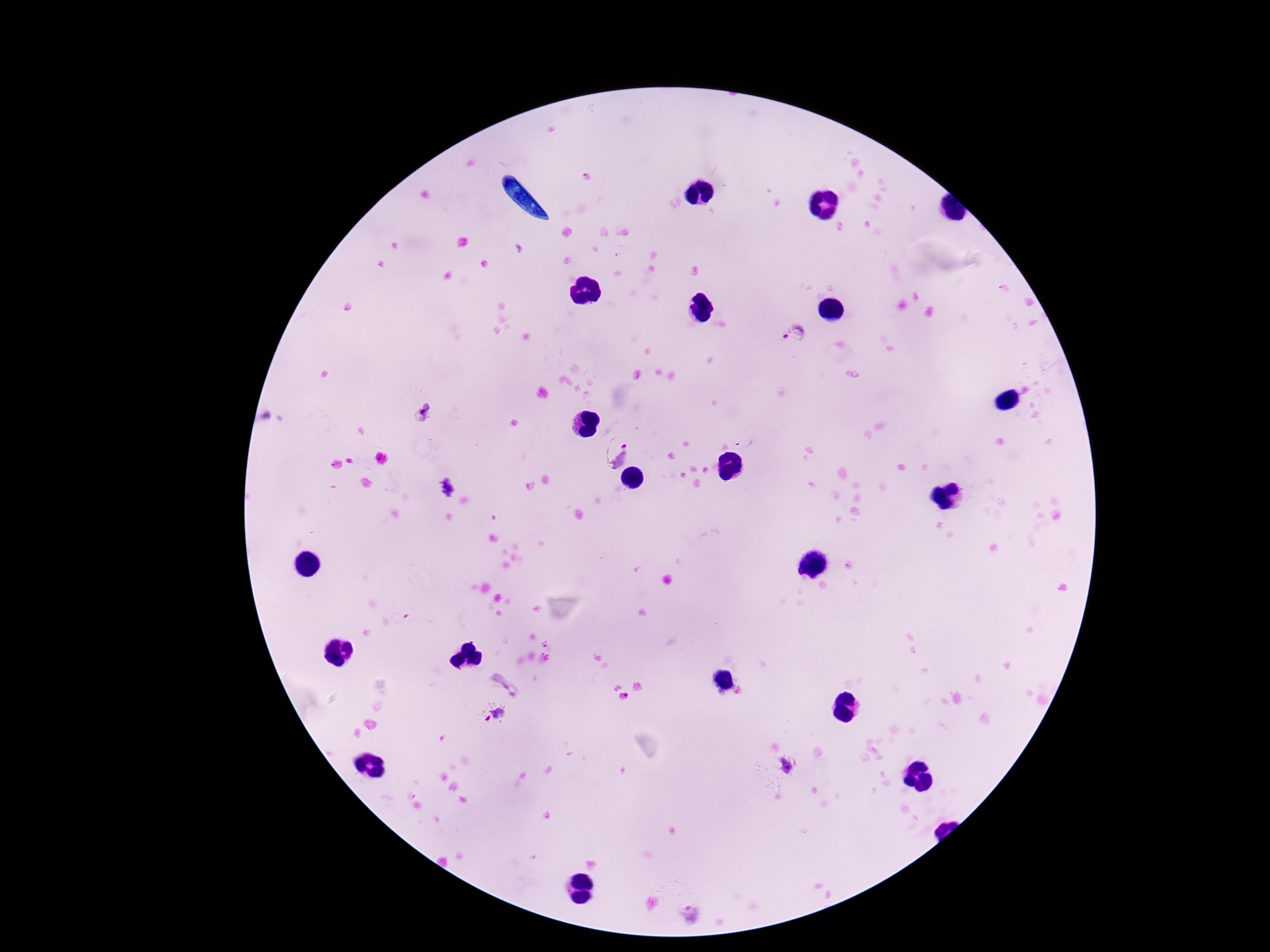

image_size: 1270×952 pixels
field_of_view: single
patient_malaria_status: infected
plasmodium_parasite_locations: 'approximate centers as {x, y} in pixels: {795, 336}, {424, 413}, {615, 451}, {445, 487}, {506, 684}, {493, 713}, {789, 765}, {690, 915}'
preparation: thick blood film
magnification: 100x
stain: Giemsa
capture: smartphone camera through the microscope eyepiece